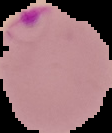

Summary:
  - Image size: 112×133 pixels
  - Image type: segmented cell region with the area outside set to black
  - Malaria status: parasitized
  - Preparation: thin blood film